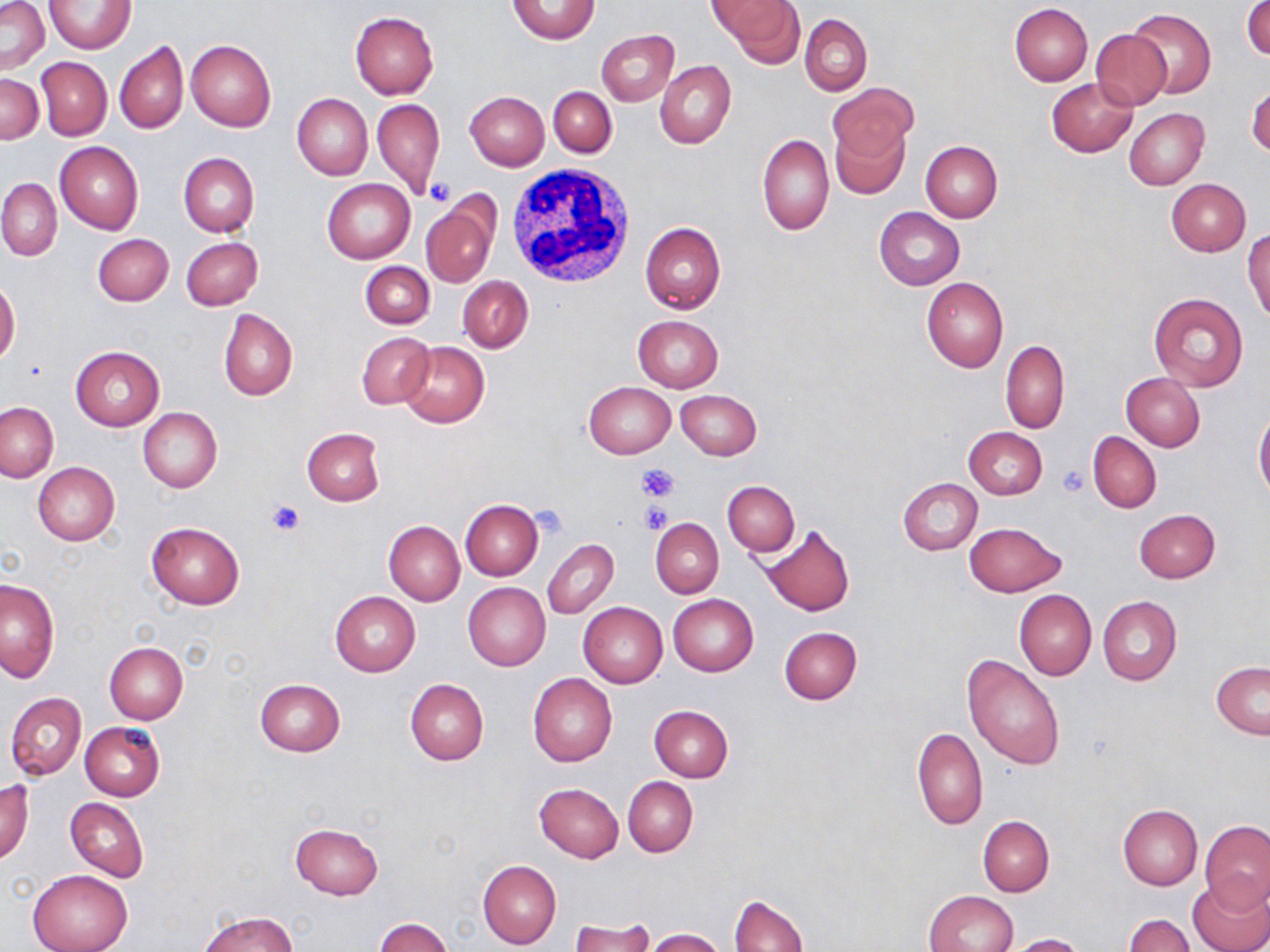
Summary:
  - Coordinate format: approximate bounding boxes as (x1,y1)-(x2,y2) corner pairs in pixels
  - Platelet locations: (427,179)-(456,206), (639,463)-(679,502), (1057,465)-(1090,496), (263,498)-(306,536), (640,503)-(671,533), (529,508)-(568,540)
  - Uninfected red blood cell locations: (1,0)-(49,74), (714,0)-(804,64), (44,1)-(135,53), (506,1)-(601,45), (1244,1)-(1270,61), (1009,3)-(1093,85), (1126,7)-(1215,99), (350,12)-(438,99), (800,13)-(872,95), (1089,28)-(1171,110), (597,29)-(678,105), (187,39)-(275,132), (115,40)-(188,135), (38,57)-(111,140), (655,60)-(735,150), (0,73)-(43,143), (1046,77)-(1137,156), (827,82)-(918,160), (1246,85)-(1270,158), (549,86)-(616,156), (465,91)-(549,171), (291,94)-(372,180), (373,98)-(446,199), (1123,108)-(1208,190), (830,118)-(909,199), (758,134)-(834,236), (921,140)-(1003,222), (56,141)-(143,235), (178,152)-(258,237), (0,179)-(61,260), (322,179)-(416,263), (1167,179)-(1251,256), (422,197)-(500,290), (874,207)-(965,290), (640,221)-(726,314), (1244,228)-(1270,321), (92,233)-(174,307), (181,237)-(262,311), (360,261)-(434,330), (458,276)-(533,352), (921,277)-(1008,372), (0,279)-(19,367), (1149,293)-(1249,391), (218,308)-(298,400), (632,315)-(724,393), (357,332)-(435,409), (1000,339)-(1069,433), (399,342)-(489,428), (70,346)-(164,430), (1122,373)-(1205,451), (584,381)-(675,458), (675,390)-(762,460), (1,402)-(58,481), (138,407)-(222,493), (1254,409)-(1270,502), (963,427)-(1046,499), (301,428)-(385,506), (1088,432)-(1161,512), (32,462)-(120,545), (898,477)-(982,556), (723,481)-(799,556), (461,499)-(543,581), (1134,509)-(1220,583), (651,519)-(724,598), (383,521)-(464,606), (146,522)-(245,609), (964,522)-(1066,597), (757,525)-(855,616), (543,538)-(619,619), (1,579)-(59,682), (463,582)-(551,671), (1014,590)-(1096,681), (330,591)-(421,676), (668,594)-(758,675), (1097,595)-(1181,685), (578,602)-(667,688), (779,627)-(862,703), (105,641)-(188,724), (962,655)-(1065,770), (1211,661)-(1270,738), (528,672)-(617,766), (255,679)-(346,757), (405,679)-(488,764), (5,692)-(85,780), (649,704)-(733,782), (80,721)-(165,800), (912,727)-(988,831), (623,776)-(698,856), (0,778)-(33,864), (535,783)-(624,861), (65,797)-(149,882), (1118,805)-(1202,889), (977,815)-(1055,895), (1201,820)-(1269,911), (290,822)-(383,899), (478,860)-(562,950), (28,870)-(131,952), (1188,877)-(1270,952), (926,890)-(1018,952), (730,893)-(807,952), (198,911)-(300,952), (1124,914)-(1195,951), (374,917)-(454,952), (568,918)-(657,950), (645,928)-(726,952), (1003,932)-(1087,952)
  - White blood cell locations: (505,167)-(636,289)
  - Slide-level diagnosis: negative for blood parasites
  - Magnification: 1000x
  - Modality: light microscopy
  - Field of view: single
  - Stain: May-Grünwald-Giemsa
  - Preparation: thin blood film
  - Image size: 1270×952 pixels